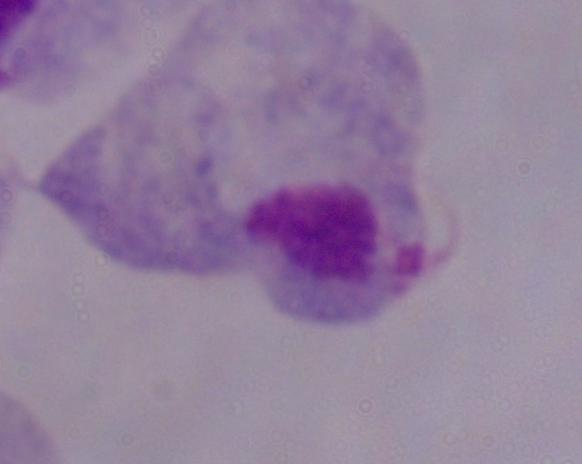

Photomicrograph. A trichomonad is seen. Captured at 1000x magnification.